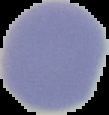

image size = 109×115 pixels
preparation = thin blood film
result = no Plasmodium parasites seen
image type = segmented cell region on a black background